Assess this cell for malaria.
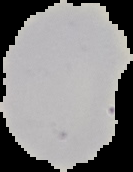

It is uninfected.

Summary:
  - Image size: 133×172 pixels
  - Preparation: thin blood smear
  - Image type: segmented cell region with the area outside set to black